State which parasite is depicted.
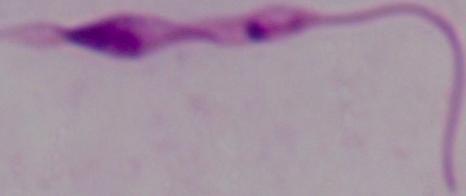

Leishmania.

modality: photomicrograph
magnification: 1000x